Classify this cell by malaria status.
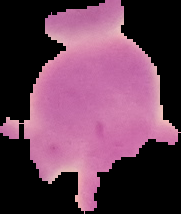
It is uninfected.

Segmented cell region on a black background. Image is 181×214 pixels. From a thin blood film.